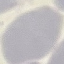
Summary:
  - Malaria status: uninfected
  - Image type: cell patch, automatically extracted from a larger field of view and resized to 64 × 64 pixels
  - Preparation: thin smear
  - Stain: Giemsa
  - Capture: smartphone through the microscope eyepiece